State which parasite is depicted.
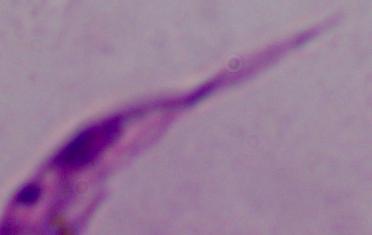
Leishmania.

{
  "modality": "photomicrograph",
  "magnification": "1000x"
}